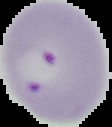

Summary:
  - Image type: segmented cell region on a black background
  - Result: Plasmodium parasites detected
  - Preparation: thin blood film
  - Image size: 112×127 pixels